Give the extent of all Plasmodium falciparum-infected red blood cells.
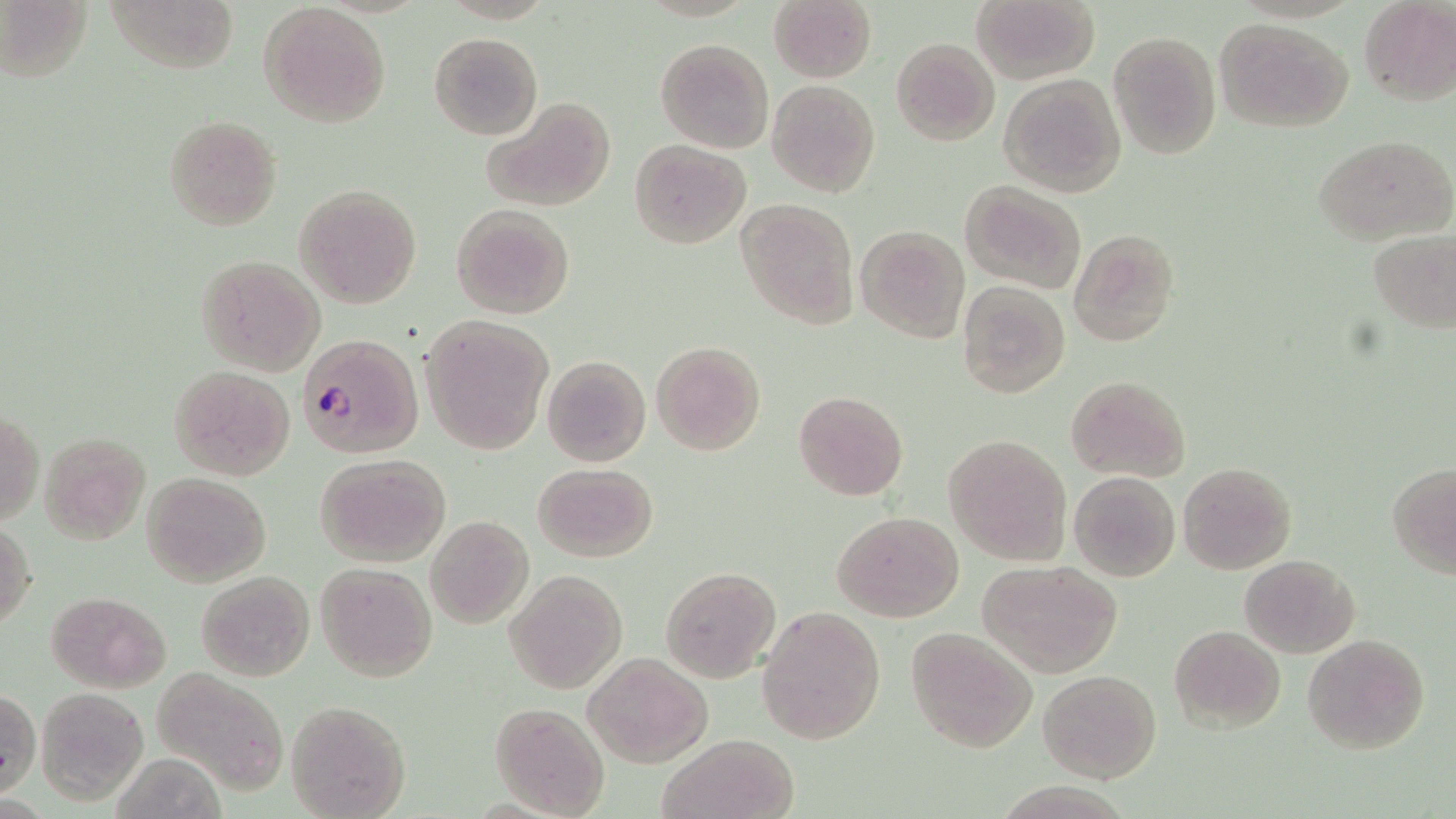

Approximate bounding boxes as (x1,y1)-(x2,y2) corner pairs in pixels.
Plasmodium falciparum-infected red blood cells: (296,333)-(422,460).

Uninfected red blood cell locations: (2,0)-(89,83), (104,0)-(238,76), (768,0)-(876,83), (1359,0)-(1455,107), (973,1)-(1097,84), (257,4)-(393,128), (1214,17)-(1353,132), (1108,30)-(1221,159), (430,32)-(541,140), (655,37)-(774,154), (891,37)-(1000,146), (999,72)-(1127,197), (767,80)-(880,199), (480,96)-(615,212), (163,114)-(283,232), (1314,135)-(1455,245), (631,140)-(748,247), (961,180)-(1089,295), (293,184)-(422,310), (734,198)-(860,329), (450,202)-(575,319), (855,224)-(970,343), (1068,228)-(1179,348), (1367,230)-(1455,333), (195,254)-(326,376), (957,281)-(1070,400), (418,313)-(555,455), (651,341)-(766,456), (540,355)-(651,468), (168,365)-(295,480), (1066,375)-(1190,483), (793,390)-(908,502), (1,409)-(43,527), (40,431)-(150,543), (943,435)-(1070,565), (315,453)-(451,567), (532,462)-(657,562), (1179,463)-(1298,574), (1388,465)-(1456,576), (1068,471)-(1180,582), (143,473)-(271,586), (832,511)-(964,623), (426,515)-(534,628), (1,521)-(36,631), (1239,553)-(1360,657), (977,559)-(1123,678), (315,562)-(437,681), (660,566)-(781,682), (196,570)-(315,680), (505,570)-(627,693), (46,591)-(171,692), (758,606)-(886,745), (1167,624)-(1285,734), (906,629)-(1037,752), (1303,633)-(1430,755), (583,653)-(712,767), (153,665)-(291,796), (1038,669)-(1162,783), (35,686)-(151,805), (1,691)-(40,797), (286,700)-(411,818), (490,702)-(611,819), (658,732)-(799,819). Slide-level diagnosis: Plasmodium falciparum. One field of a larger specimen. Image is 1456×819 pixels. May-Grünwald-Giemsa-stained preparation. Thin blood film. 1000x magnification. Light microscopy.